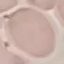

result = no malaria parasites seen
stain = Giemsa
capture = smartphone through the microscope eyepiece
preparation = thin smear
image type = automatically extracted cell patch, resized to 64 × 64 pixels